Locate the red blood cells and classify each one as P. falciparum-infected, uninfected, or of indeterminate infection status.
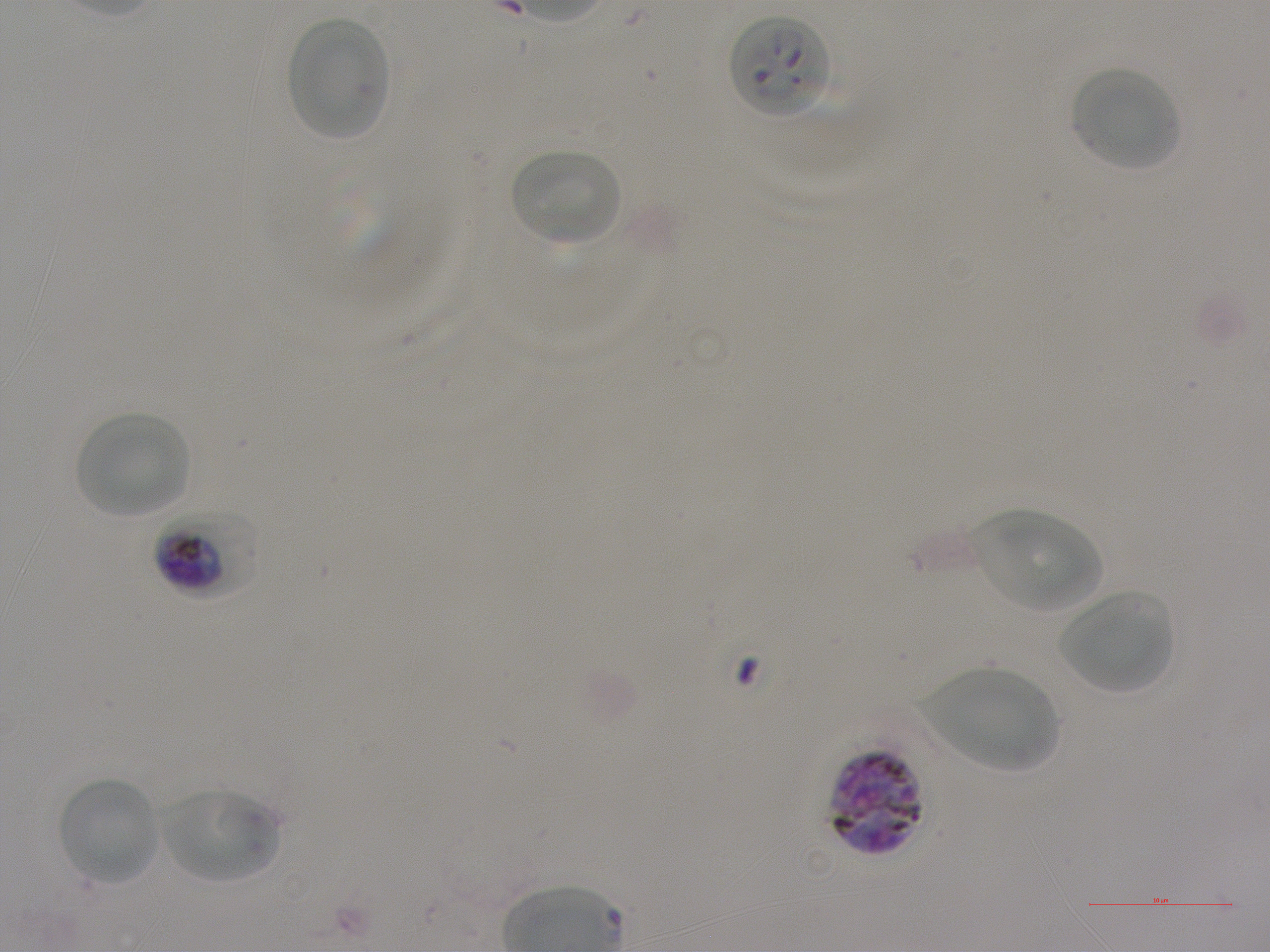
Approximate bounding boxes as (x1, y1, x2, y2) in pixels. Not every red blood cell is marked. A life-cycle stage — or a range of stages, where the recorded stages span more than one — follows each staged infected red blood cell.
Infected red blood cells: (729, 15, 831, 119); (155, 507, 258, 596) early trophozoite to early schizont; (830, 749, 923, 856).
Uninfected red blood cells: (285, 17, 388, 141), (1070, 66, 1181, 172), (511, 148, 622, 245), (76, 412, 190, 519), (972, 510, 1102, 613), (1060, 592, 1174, 693), (923, 667, 1059, 770), (59, 776, 160, 885), (162, 789, 279, 883).
No red blood cells of indeterminate infection status observed.

Donor blood group A+. 100x objective under oil immersion, numerical aperture 1.25. Single field of view. Image is 1270×952 pixels. Thin blood film. Static in-vitro culture of P. falciparum strain NF54. Giemsa-stained preparation.